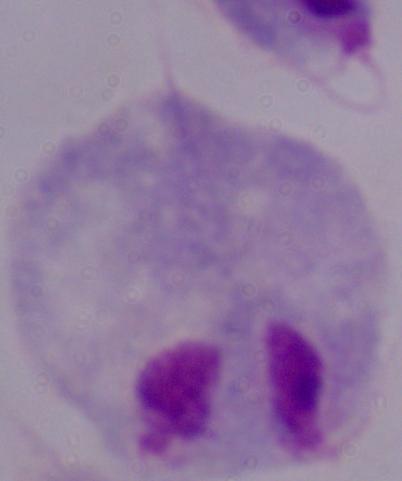
1000x magnification. A trichomonad is shown. Micrograph.